Assess for Plasmodium parasites.
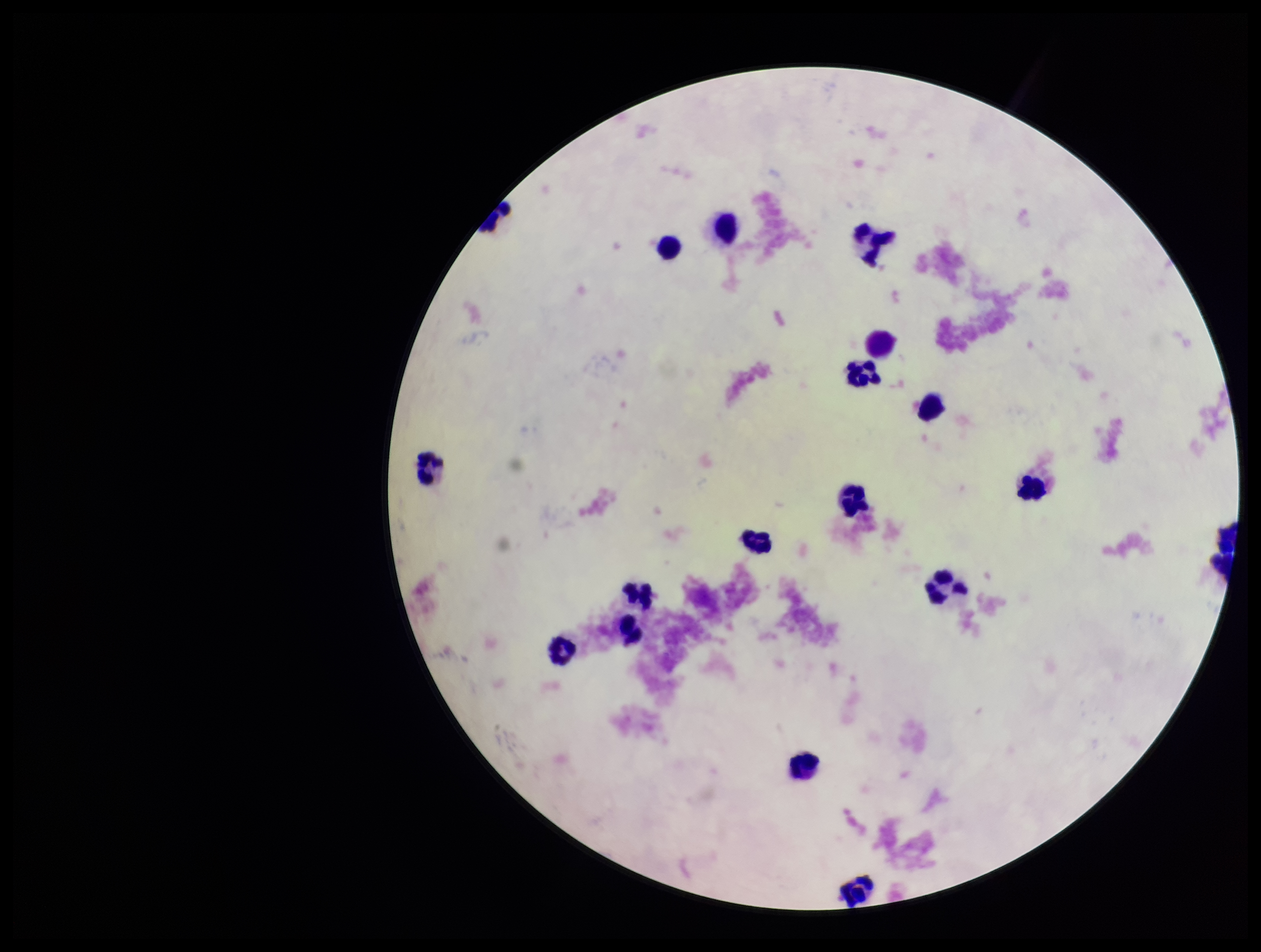

None detected.

parasite count = 0
leukocyte count = 18
stain = Giemsa
preparation = thick
field of view = one from this slide
patient malaria status = negative
image size = 1261×952 pixels
capture = smartphone photograph through the microscope eyepiece